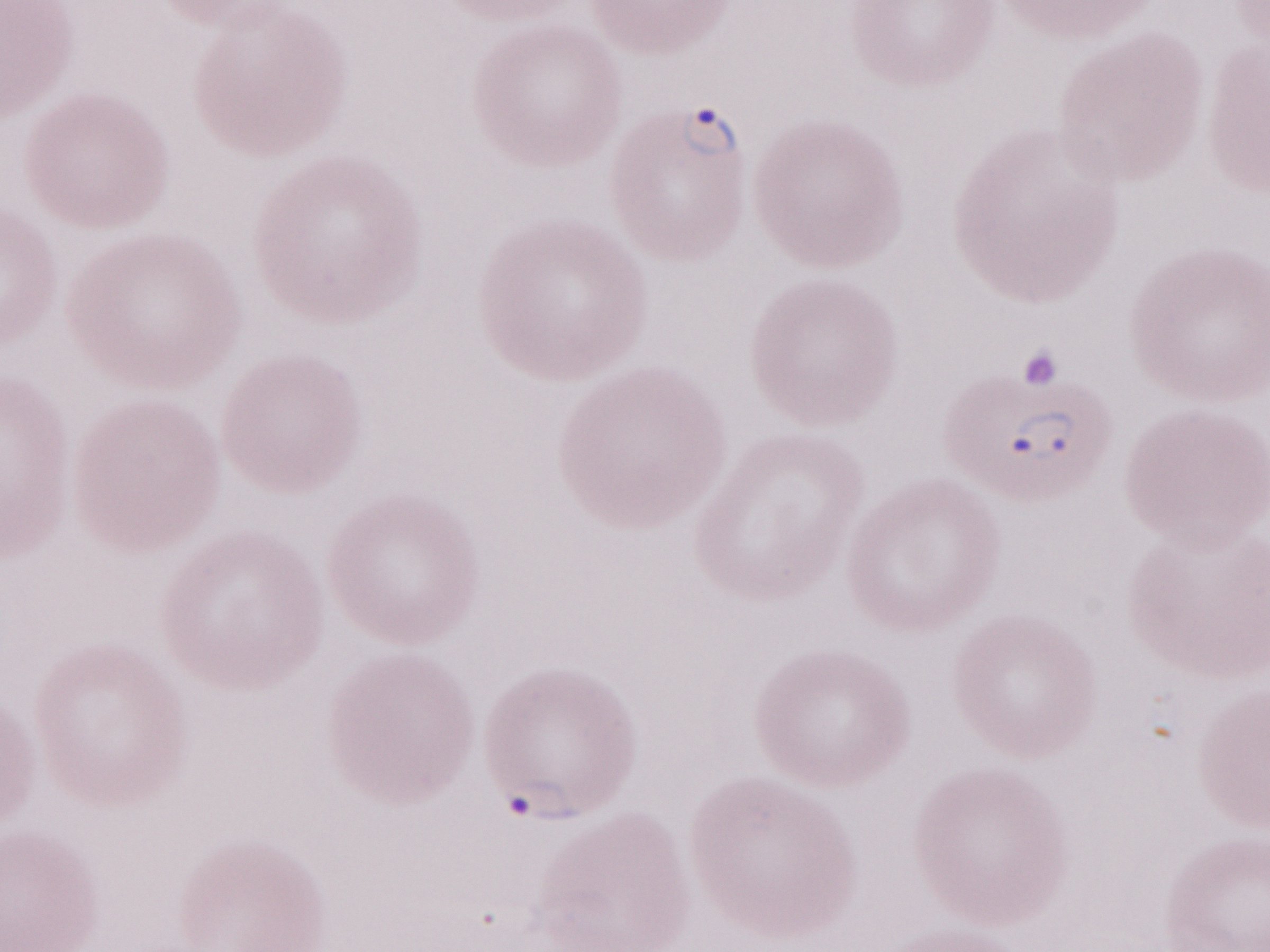 One field of this slide. Image is 1270×952 pixels. Magnification: 1,000x. Thin peripheral-blood smear. Patient-level malaria diagnosis: positive. May-Grünwald-Giemsa (MGG) stain. Olympus BX43 microscope, Olympus DP73 camera.